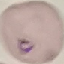
Result: malaria parasites detected. Automatically extracted cell patch, resized to 64 × 64 pixels. Giemsa stain. Thin blood smear. Photographed with a smartphone camera at the microscope eyepiece.